Comment on the morphology of the red blood cells.
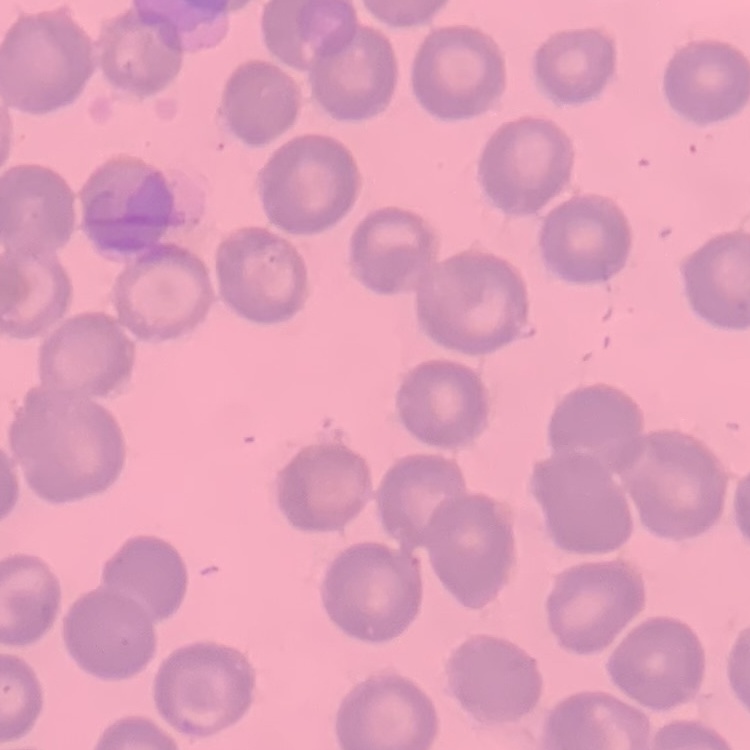

No rouleaux formation.

Field's or Giemsa stain. One tile cut from a larger photomicrograph. Thin blood smear.